State which parasite is depicted.
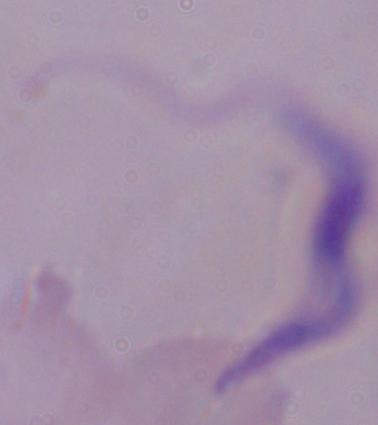

This is a trypanosome.

Summary:
  - Magnification: 1000x
  - Modality: photomicrograph